Describe the morphology of the erythrocytes.
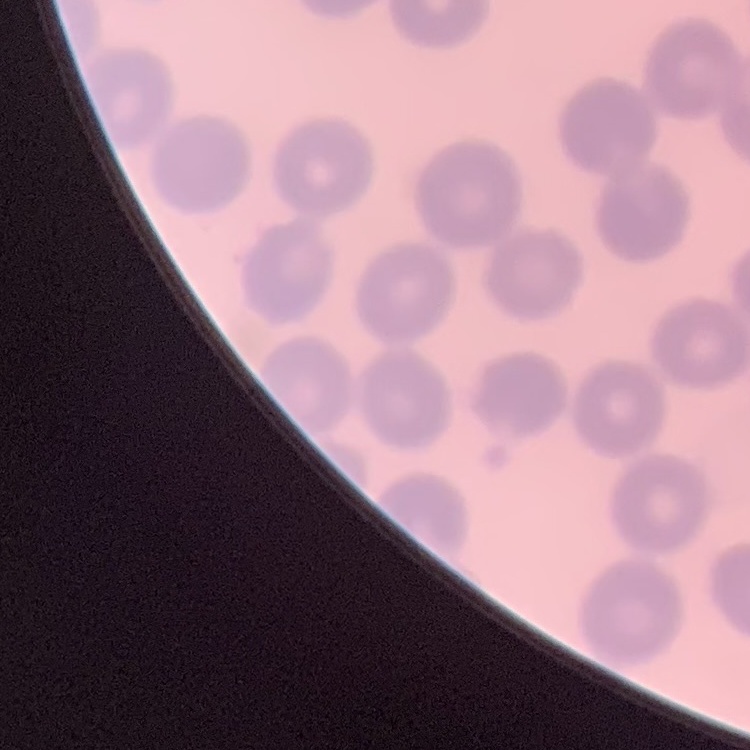

They show no rouleaux formation.

One tile cut from a larger photomicrograph. Thin blood smear. Stained with either Field's or Giemsa.